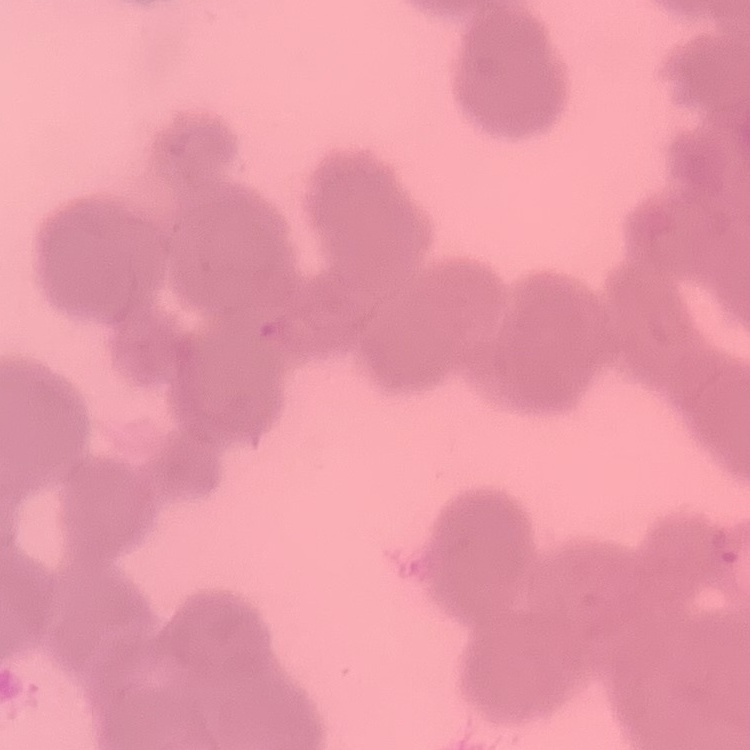

erythrocyte morphology = rouleaux formation
stain = Field's or Giemsa
image type = one tile cut from a larger photomicrograph
preparation = thin blood film